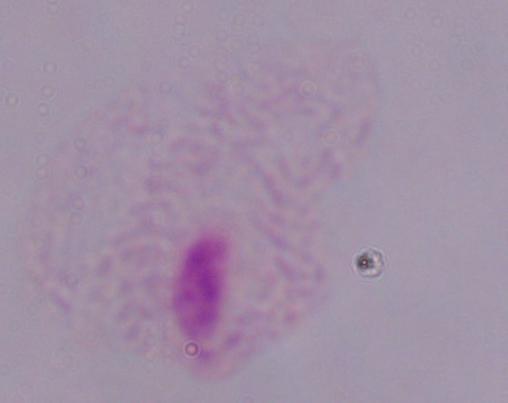

1000x magnification. Photomicrograph. A trichomonad is shown.